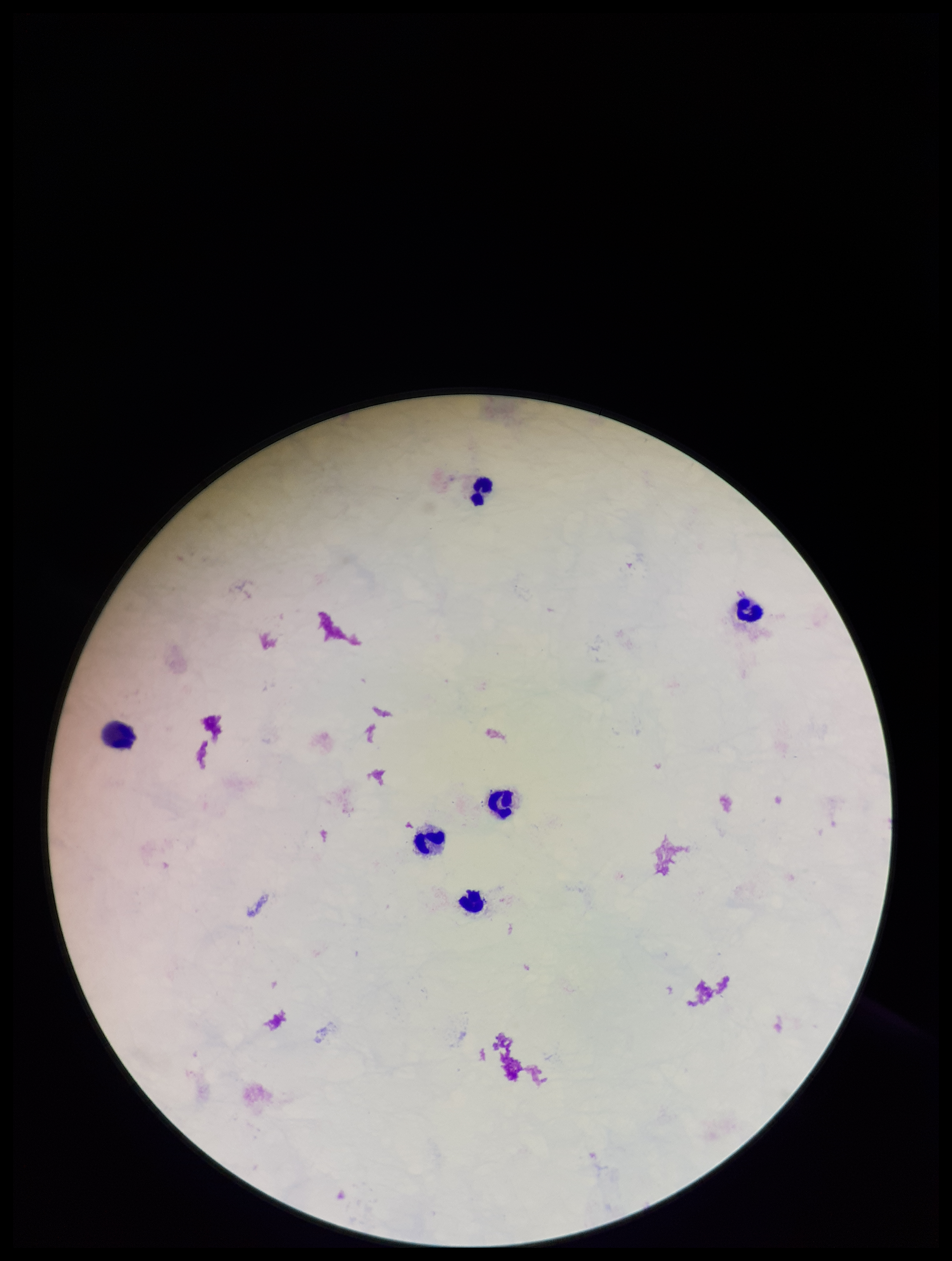
Summary:
  - Preparation: thick smear
  - Patient malaria status: negative
  - Image size: 952×1261 pixels
  - Field of view: single
  - Capture: smartphone photograph through the microscope eyepiece
  - Plasmodium parasites: none detected
  - Leukocyte count: 6
  - Stain: Giemsa
  - Parasite count: 0